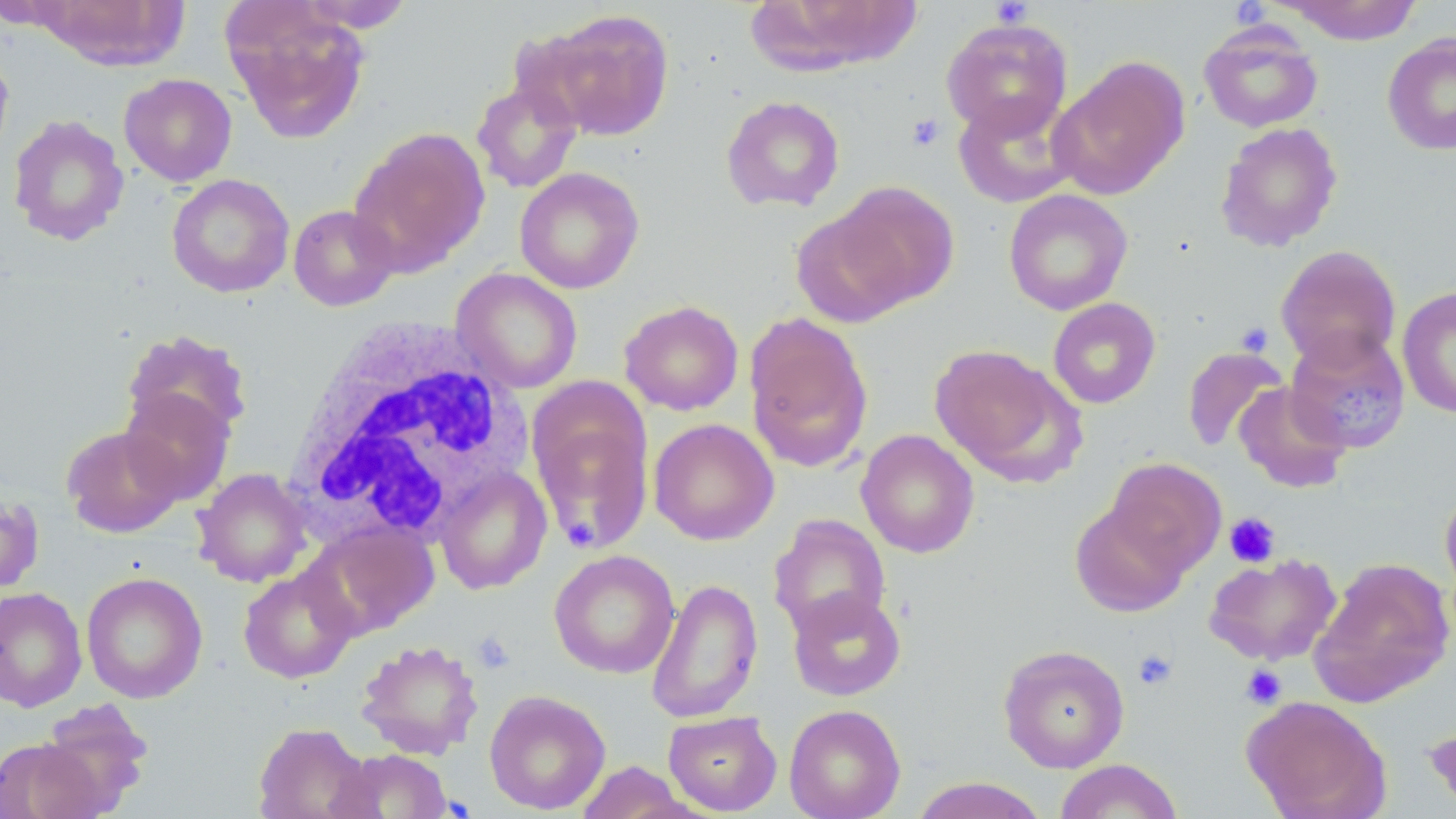
{
  "slide_level_diagnosis": "no evidence of blood parasites",
  "platelet_locations": "approximate bounding boxes as [x1, y1, x2, y2] in pixels: [990, 0, 1033, 28], [1230, 1, 1271, 29], [907, 114, 945, 151], [1235, 322, 1274, 357], [1224, 512, 1280, 568], [563, 515, 599, 551], [472, 631, 514, 673], [1133, 649, 1177, 690], [1240, 664, 1287, 709]",
  "field_of_view": "one of a larger specimen",
  "magnification": "1000x",
  "preparation": "thin blood film",
  "white_blood_cell_locations": "approximate bounding boxes as [x1, y1, x2, y2] in pixels: [285, 318, 530, 546]",
  "image_size": "1456×819 pixels",
  "uninfected_red_blood_cell_locations": "approximate bounding boxes as [x1, y1, x2, y2] in pixels: [30, 0, 190, 71], [294, 1, 415, 33], [1276, 1, 1424, 44], [222, 3, 371, 145], [540, 9, 675, 141], [940, 17, 1073, 140], [1198, 22, 1324, 133], [1382, 32, 1456, 155], [0, 46, 14, 167], [1049, 55, 1190, 200], [119, 73, 237, 186], [471, 79, 582, 193], [952, 91, 1080, 208], [720, 95, 846, 213], [7, 114, 129, 246], [1215, 122, 1343, 252], [349, 127, 490, 275], [514, 167, 645, 294], [167, 174, 295, 298], [831, 180, 960, 310], [1003, 189, 1133, 315], [288, 204, 398, 311], [790, 208, 916, 328], [1275, 245, 1402, 371], [451, 268, 583, 394], [1397, 285, 1455, 419], [1047, 297, 1161, 408], [620, 300, 744, 415], [744, 313, 874, 473], [122, 329, 253, 442], [1284, 329, 1411, 454], [929, 344, 1082, 485], [1181, 346, 1289, 453], [1233, 381, 1352, 494], [119, 388, 235, 505], [529, 398, 654, 552], [649, 418, 778, 545], [61, 424, 185, 538], [856, 429, 980, 558], [1104, 457, 1227, 576], [434, 466, 552, 595], [192, 468, 313, 587], [1440, 487, 1456, 601], [0, 492, 45, 595], [1070, 500, 1191, 617], [769, 513, 891, 638], [305, 518, 440, 636], [549, 549, 680, 678], [1204, 552, 1342, 666], [1308, 558, 1455, 707], [238, 566, 358, 684], [81, 571, 208, 704], [646, 576, 763, 724], [0, 586, 87, 712], [787, 587, 906, 701], [355, 638, 484, 760], [997, 643, 1130, 773], [484, 690, 611, 814], [1241, 694, 1392, 819], [36, 699, 155, 816], [784, 704, 906, 819], [663, 711, 783, 816], [1424, 717, 1456, 814], [253, 722, 373, 819], [0, 737, 104, 819], [330, 748, 454, 819], [1053, 759, 1184, 818], [572, 760, 697, 818], [909, 776, 1050, 819]",
  "modality": "light microscopy",
  "stain": "May-Grünwald-Giemsa"
}